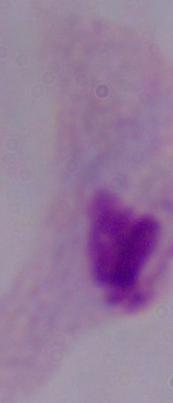

identification = trichomonad
modality = micrograph
magnification = 1000x